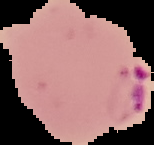

From a thin blood film. Malaria status: parasitized. The area outside the segmented cell region is set to black. Image is 154×145 pixels.